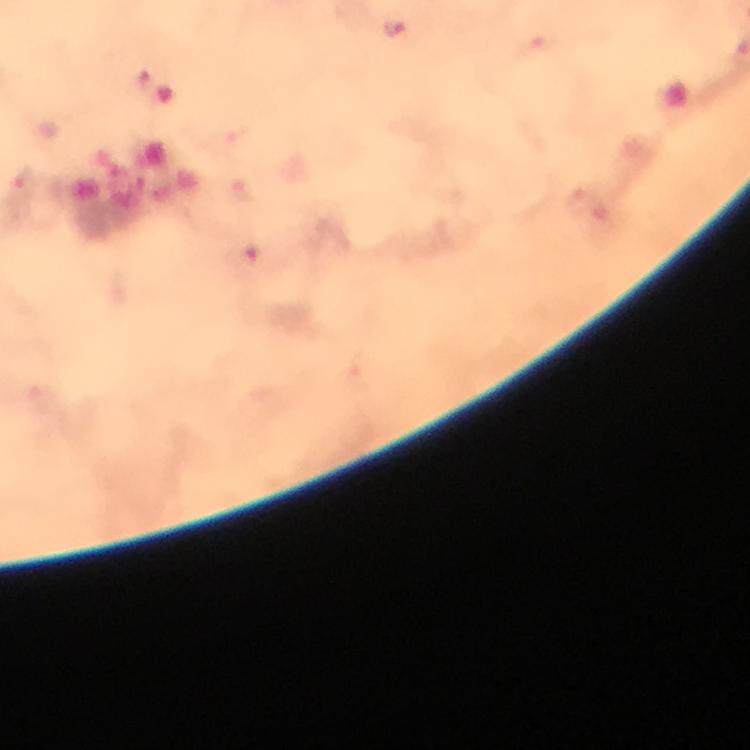
Approximate centers as [x, y] in pixels. Malaria parasite locations: [394, 30]. Smartphone photograph taken through a microscope. Immersion oil was used. Thick blood smear. Cropped region of a single field of view. 100x magnification. Giemsa-stained preparation. Image is 750×750 pixels. From a malaria diagnostic workup.